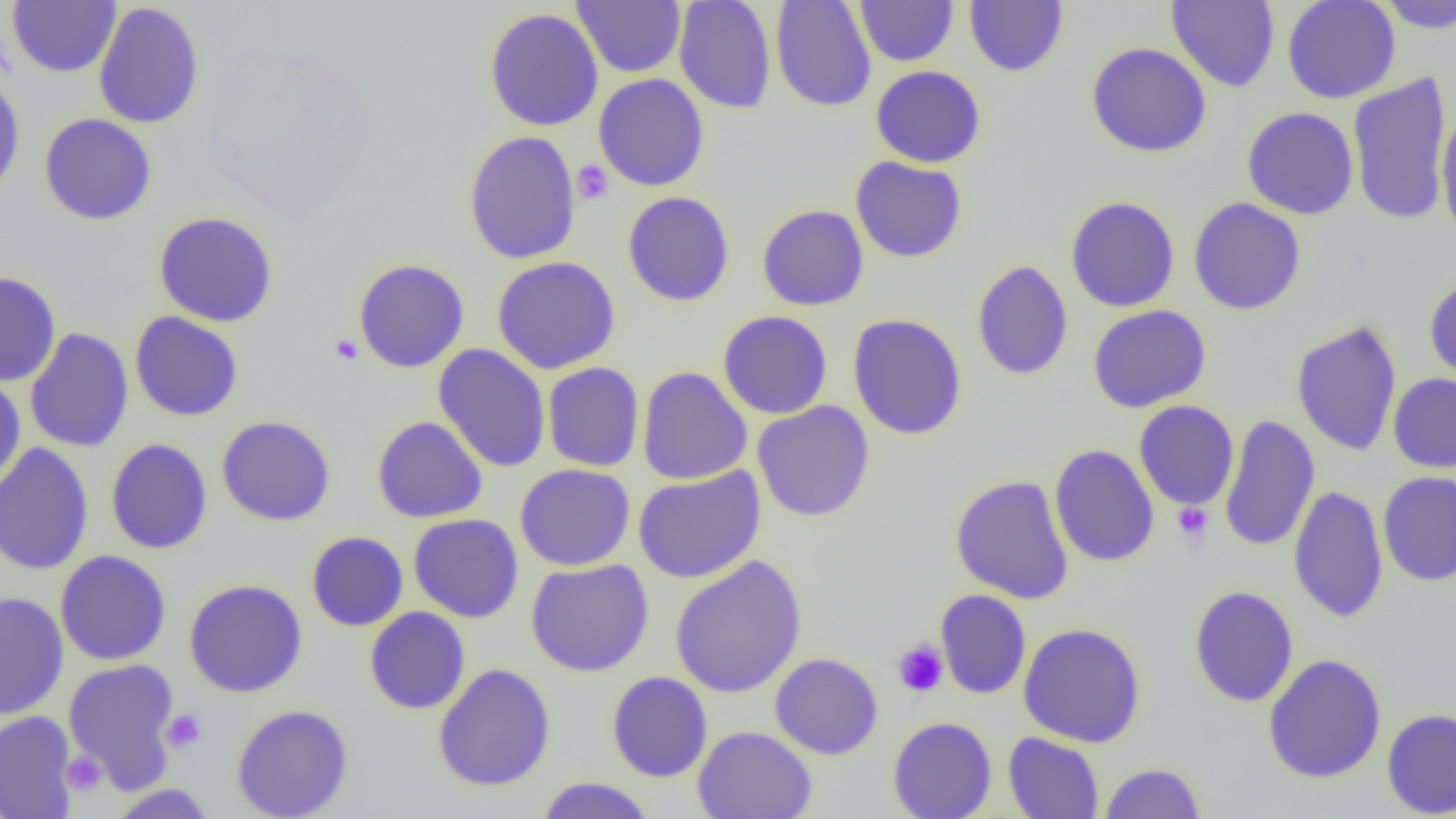

Summary:
  - Coordinate format: approximate bounding boxes as (x1, y1, x2, y2) in pixels
  - Uninfected red blood cell locations: (7, 0, 121, 77), (572, 0, 686, 78), (674, 0, 776, 114), (770, 0, 876, 112), (854, 0, 959, 66), (1166, 0, 1280, 92), (1282, 0, 1401, 103), (1375, 0, 1456, 34), (93, 1, 205, 130), (963, 1, 1069, 77), (484, 7, 603, 131), (1086, 42, 1212, 158), (870, 66, 986, 168), (1347, 70, 1451, 227), (0, 72, 26, 201), (594, 74, 709, 192), (1242, 107, 1359, 220), (1436, 107, 1456, 241), (39, 113, 157, 225), (463, 130, 581, 265), (850, 157, 967, 263), (622, 191, 735, 307), (1065, 195, 1180, 313), (1188, 197, 1306, 315), (757, 204, 869, 311), (153, 211, 278, 327), (492, 256, 621, 375), (353, 259, 470, 373), (971, 260, 1073, 381), (0, 271, 61, 387), (1423, 277, 1456, 386), (1088, 305, 1211, 413), (718, 310, 833, 419), (130, 311, 244, 421), (848, 313, 967, 441), (1290, 320, 1402, 457), (24, 327, 134, 453), (434, 344, 551, 473), (542, 362, 645, 472), (637, 366, 752, 485), (0, 373, 26, 491), (1388, 373, 1456, 473), (752, 401, 875, 522), (1134, 401, 1239, 510), (216, 415, 336, 526), (1218, 415, 1319, 553), (371, 416, 488, 523), (106, 438, 213, 554), (0, 442, 94, 576), (1049, 444, 1159, 568), (515, 464, 635, 571), (632, 466, 766, 583), (1378, 471, 1456, 586), (949, 475, 1074, 604), (1288, 484, 1388, 623), (409, 513, 524, 623), (306, 531, 409, 631), (55, 550, 171, 666), (669, 555, 807, 699), (525, 559, 654, 677), (184, 578, 308, 698), (1188, 585, 1299, 707), (935, 589, 1031, 699), (0, 592, 69, 720), (365, 606, 470, 714), (1018, 622, 1146, 747), (770, 653, 883, 759), (1262, 653, 1387, 784), (63, 658, 180, 792), (433, 663, 556, 792), (607, 671, 713, 782), (231, 704, 353, 819), (1381, 708, 1456, 818), (0, 711, 79, 819), (888, 716, 997, 819), (692, 726, 816, 819), (1003, 732, 1104, 819), (1099, 762, 1206, 818), (536, 777, 656, 819), (106, 783, 219, 817)
  - Platelet locations: (572, 160, 613, 205), (330, 334, 363, 365), (1172, 503, 1214, 545), (892, 639, 949, 697), (161, 708, 206, 753), (62, 751, 107, 796)
  - Slide-level diagnosis: no evidence of blood parasites
  - Magnification: 1000x
  - Preparation: thin blood smear
  - Modality: optical microscopy
  - Image size: 1456×819 pixels
  - Field of view: one of a larger specimen